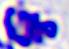
modality = photomicrograph
magnification = 400x
identification = leukocyte